Give the position of every leukocyte visible.
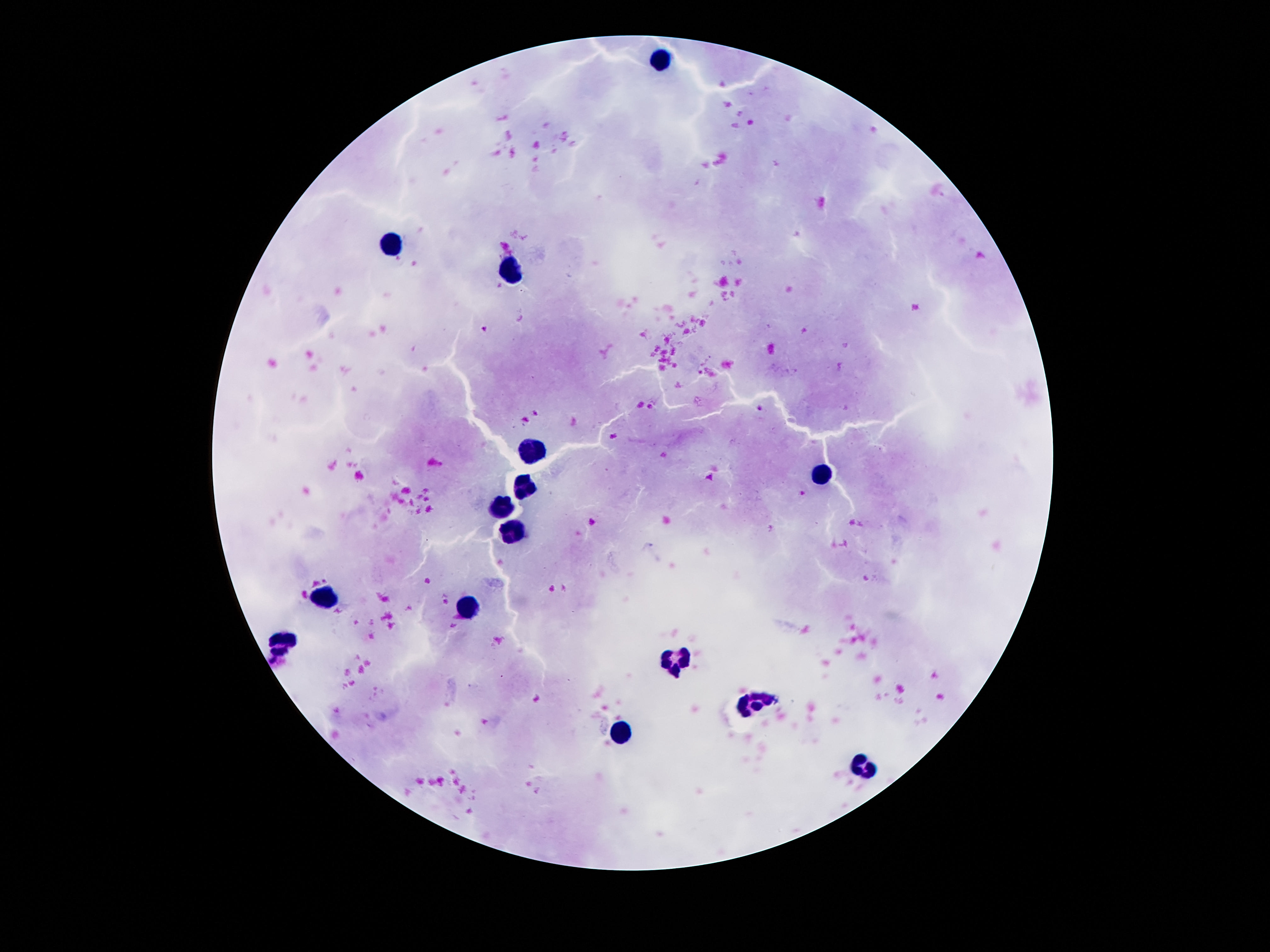
Approximate object centers, in pixels from the top-left corner.
Leukocytes: (x=660, y=61), (x=387, y=244), (x=508, y=273), (x=532, y=452), (x=823, y=473), (x=526, y=489), (x=500, y=508), (x=510, y=532), (x=328, y=596), (x=463, y=606), (x=279, y=643), (x=674, y=662), (x=754, y=699), (x=619, y=734), (x=866, y=768).

Giemsa stain. Patient malaria status: negative. Thick blood smear. Photographed through the microscope eyepiece with a smartphone camera. Single field of view. 100x magnification. Image is 1270×952 pixels.